Name the parasite shown.
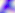
Toxoplasma gondii.

Captured at 400x magnification. Photomicrograph.